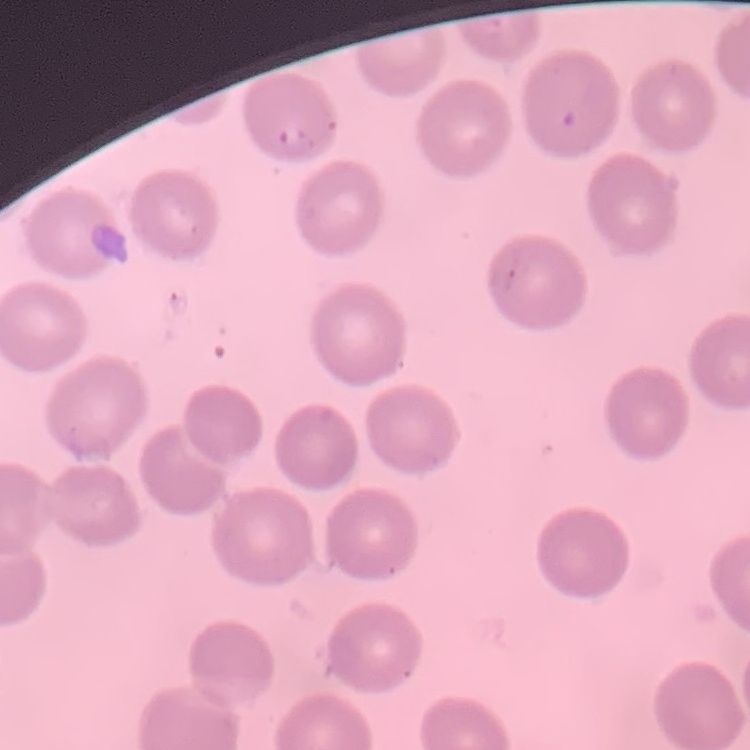
The red blood cells exhibit no rouleaux formation. One tile cut from a larger photomicrograph. Thin blood film. Field's or Giemsa stain.